Assess this cell for malaria.
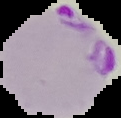

It is parasitized.

From a thin blood smear. Cell region segmented out of the field of view; the surrounding area is masked to black. Image is 121×118 pixels.